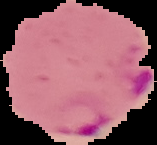 Malaria status: parasitized. Cell region segmented out of the field of view; the surrounding area is masked to black. Image is 157×145 pixels. From a thin blood smear.